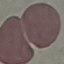 Result: no malaria parasites seen. Cell patch, automatically extracted from a larger field of view and resized to 64 × 64 pixels. Acquired by smartphone through the microscope eyepiece. Thin smear of blood. Giemsa-stained preparation.